Classify this cell by malaria status.
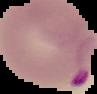

Parasitized.

From a thin blood film. Image is 97×94 pixels. Segmented cell region on a black background.